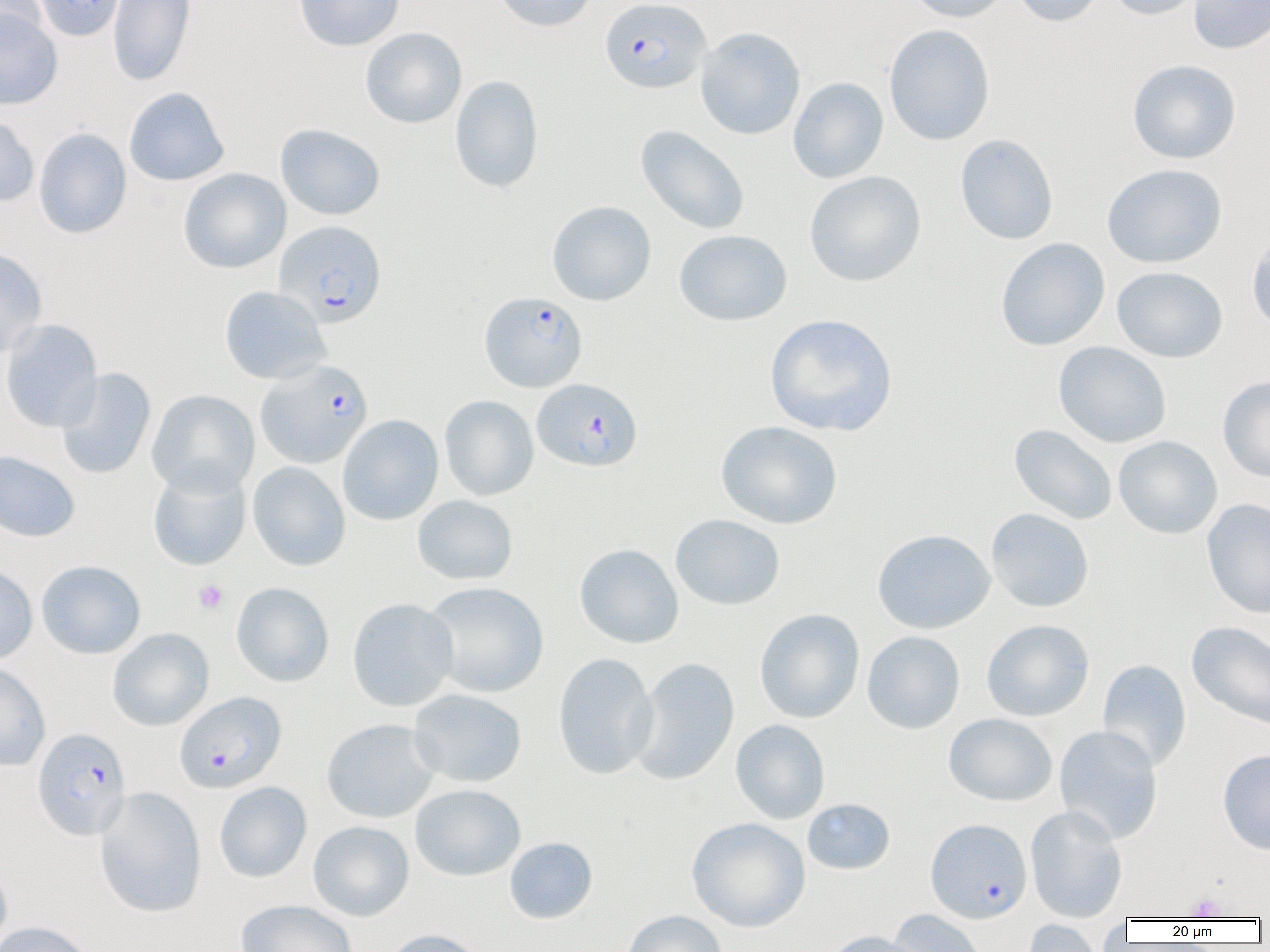
Approximate bounding boxes as named x1/y1/x2/y2 corners in pixels. Uninfected red blood cell locations: (x1=0, y1=0, x2=46, y2=47), (x1=33, y1=0, x2=124, y2=41), (x1=108, y1=0, x2=195, y2=86), (x1=294, y1=0, x2=404, y2=52), (x1=491, y1=0, x2=599, y2=32), (x1=903, y1=0, x2=1012, y2=23), (x1=1011, y1=0, x2=1106, y2=27), (x1=1105, y1=0, x2=1208, y2=21), (x1=1188, y1=0, x2=1270, y2=54), (x1=0, y1=7, x2=62, y2=110), (x1=884, y1=23, x2=995, y2=145), (x1=360, y1=27, x2=467, y2=129), (x1=695, y1=27, x2=806, y2=140), (x1=1126, y1=59, x2=1242, y2=164), (x1=449, y1=75, x2=544, y2=193), (x1=787, y1=77, x2=889, y2=184), (x1=124, y1=87, x2=229, y2=186), (x1=0, y1=113, x2=39, y2=207), (x1=275, y1=123, x2=386, y2=220), (x1=635, y1=125, x2=750, y2=235), (x1=33, y1=128, x2=132, y2=239), (x1=955, y1=134, x2=1058, y2=245), (x1=1102, y1=163, x2=1227, y2=268), (x1=178, y1=168, x2=291, y2=274), (x1=804, y1=171, x2=926, y2=287), (x1=547, y1=200, x2=657, y2=306), (x1=1246, y1=227, x2=1270, y2=337), (x1=674, y1=229, x2=793, y2=327), (x1=995, y1=238, x2=1110, y2=351), (x1=0, y1=248, x2=47, y2=358), (x1=1112, y1=266, x2=1228, y2=362), (x1=219, y1=286, x2=331, y2=384), (x1=764, y1=313, x2=898, y2=437), (x1=1, y1=319, x2=103, y2=433), (x1=1053, y1=341, x2=1172, y2=448), (x1=56, y1=367, x2=156, y2=479), (x1=1218, y1=375, x2=1270, y2=483), (x1=147, y1=389, x2=259, y2=497), (x1=440, y1=395, x2=539, y2=501), (x1=337, y1=414, x2=443, y2=525), (x1=716, y1=421, x2=843, y2=529), (x1=1009, y1=424, x2=1118, y2=525), (x1=1113, y1=436, x2=1223, y2=539), (x1=0, y1=450, x2=80, y2=543), (x1=248, y1=461, x2=350, y2=571), (x1=148, y1=464, x2=251, y2=570), (x1=412, y1=495, x2=518, y2=585), (x1=1202, y1=498, x2=1270, y2=619), (x1=986, y1=508, x2=1094, y2=613), (x1=670, y1=514, x2=785, y2=610), (x1=872, y1=529, x2=995, y2=634), (x1=574, y1=544, x2=684, y2=649), (x1=36, y1=560, x2=146, y2=659), (x1=0, y1=564, x2=38, y2=664), (x1=422, y1=581, x2=548, y2=698), (x1=231, y1=582, x2=334, y2=687), (x1=347, y1=598, x2=458, y2=711), (x1=755, y1=608, x2=865, y2=724), (x1=981, y1=619, x2=1094, y2=721), (x1=1186, y1=621, x2=1270, y2=731), (x1=107, y1=628, x2=214, y2=731), (x1=862, y1=631, x2=965, y2=734), (x1=553, y1=653, x2=658, y2=779), (x1=628, y1=657, x2=740, y2=786), (x1=1097, y1=659, x2=1192, y2=772), (x1=0, y1=662, x2=50, y2=771), (x1=408, y1=688, x2=527, y2=788), (x1=943, y1=713, x2=1058, y2=806), (x1=321, y1=718, x2=439, y2=823), (x1=730, y1=720, x2=830, y2=823), (x1=1054, y1=725, x2=1163, y2=844), (x1=1217, y1=749, x2=1270, y2=855), (x1=214, y1=781, x2=312, y2=883), (x1=410, y1=784, x2=526, y2=881), (x1=95, y1=786, x2=206, y2=918), (x1=802, y1=798, x2=895, y2=875), (x1=1026, y1=805, x2=1127, y2=923), (x1=686, y1=817, x2=810, y2=933), (x1=308, y1=820, x2=415, y2=921), (x1=504, y1=837, x2=598, y2=924), (x1=0, y1=856, x2=13, y2=951), (x1=236, y1=899, x2=357, y2=952), (x1=886, y1=909, x2=987, y2=952), (x1=622, y1=910, x2=728, y2=952), (x1=1097, y1=914, x2=1128, y2=951), (x1=1022, y1=919, x2=1106, y2=952), (x1=0, y1=920, x2=97, y2=952), (x1=381, y1=928, x2=487, y2=952), (x1=821, y1=930, x2=930, y2=952). Plasmodium falciparum-infected red blood cell locations: (x1=600, y1=0, x2=711, y2=94), (x1=274, y1=220, x2=386, y2=329), (x1=479, y1=291, x2=587, y2=392), (x1=256, y1=360, x2=373, y2=468), (x1=532, y1=378, x2=643, y2=471), (x1=174, y1=691, x2=286, y2=794), (x1=32, y1=727, x2=130, y2=840), (x1=925, y1=818, x2=1032, y2=923). Platelet locations: (x1=194, y1=580, x2=228, y2=613), (x1=1185, y1=893, x2=1226, y2=920). Slide-level diagnosis: Plasmodium falciparum. One field of a larger specimen. Thin blood smear. Image is 1270×952 pixels. 1000x magnification. Light microscopy.